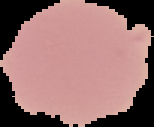
Malaria status: uninfected. From a thin blood film. Image is 154×127 pixels. Cell region segmented out of the field of view; the surrounding area is masked to black.